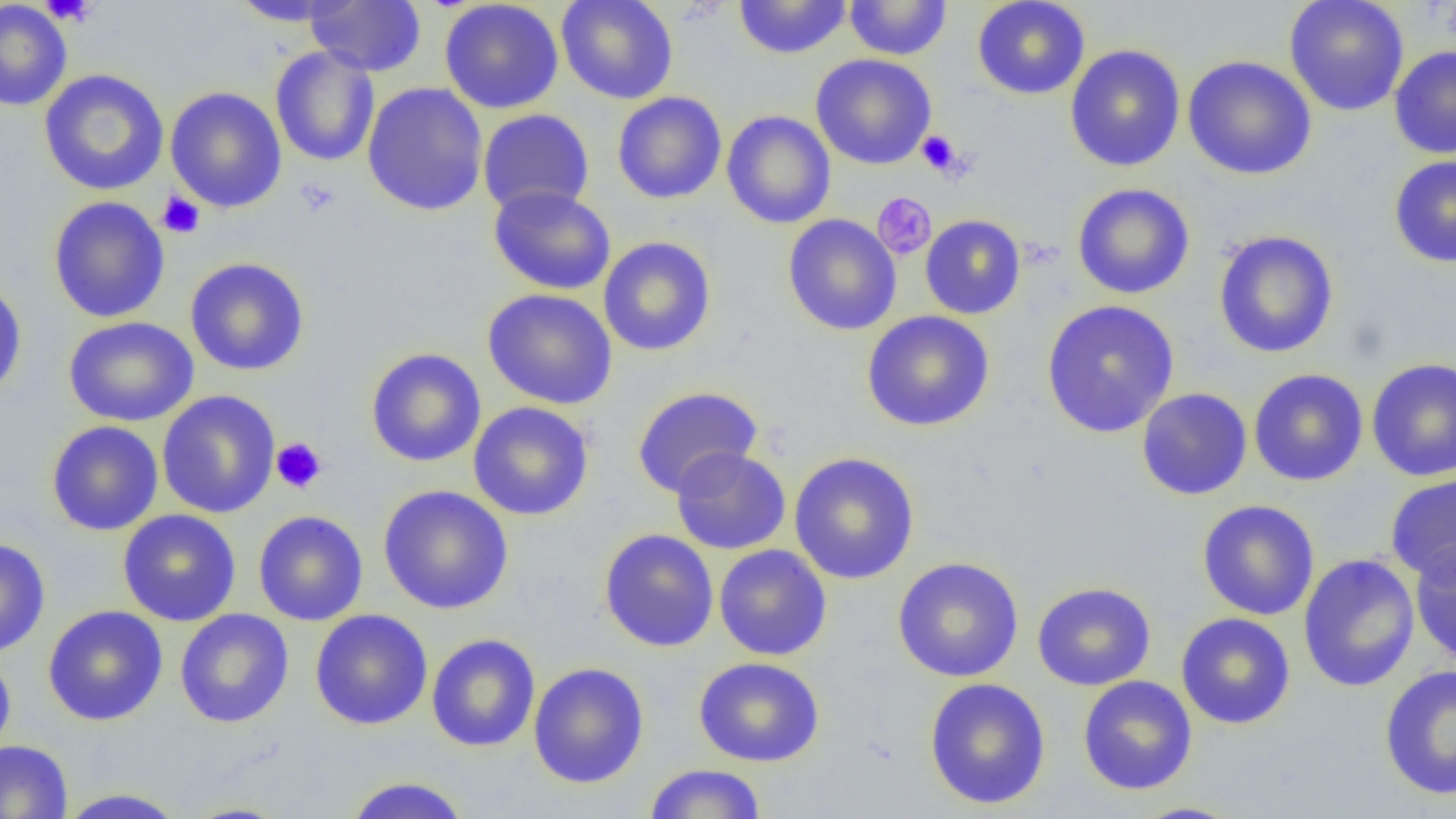

Summary:
  - Coordinate format: approximate bounding boxes as named x1/y1/x2/y2 corners in pixels
  - Uninfected red blood cell locations: (x1=228, y1=0, x2=355, y2=27), (x1=305, y1=0, x2=426, y2=76), (x1=439, y1=0, x2=564, y2=114), (x1=556, y1=0, x2=679, y2=104), (x1=733, y1=0, x2=852, y2=59), (x1=972, y1=0, x2=1091, y2=100), (x1=1284, y1=0, x2=1409, y2=116), (x1=0, y1=1, x2=72, y2=111), (x1=844, y1=1, x2=952, y2=60), (x1=1065, y1=44, x2=1185, y2=172), (x1=270, y1=46, x2=380, y2=166), (x1=1389, y1=46, x2=1456, y2=159), (x1=810, y1=53, x2=937, y2=170), (x1=1182, y1=55, x2=1317, y2=180), (x1=39, y1=69, x2=169, y2=196), (x1=362, y1=82, x2=488, y2=216), (x1=165, y1=86, x2=287, y2=213), (x1=612, y1=91, x2=727, y2=204), (x1=478, y1=109, x2=594, y2=215), (x1=722, y1=110, x2=836, y2=229), (x1=1388, y1=154, x2=1456, y2=268), (x1=1071, y1=182, x2=1196, y2=300), (x1=488, y1=185, x2=616, y2=295), (x1=47, y1=196, x2=170, y2=323), (x1=783, y1=214, x2=902, y2=335), (x1=920, y1=215, x2=1026, y2=319), (x1=1213, y1=230, x2=1339, y2=359), (x1=598, y1=236, x2=716, y2=356), (x1=185, y1=257, x2=310, y2=376), (x1=0, y1=276, x2=27, y2=402), (x1=482, y1=288, x2=618, y2=410), (x1=1040, y1=299, x2=1180, y2=438), (x1=862, y1=310, x2=995, y2=432), (x1=63, y1=316, x2=199, y2=427), (x1=366, y1=348, x2=486, y2=468), (x1=1366, y1=358, x2=1456, y2=481), (x1=1249, y1=368, x2=1368, y2=486), (x1=631, y1=386, x2=763, y2=498), (x1=1137, y1=388, x2=1252, y2=500), (x1=157, y1=390, x2=280, y2=518), (x1=468, y1=401, x2=594, y2=521), (x1=47, y1=420, x2=164, y2=536), (x1=670, y1=447, x2=791, y2=555), (x1=789, y1=452, x2=920, y2=584), (x1=1385, y1=473, x2=1456, y2=585), (x1=378, y1=484, x2=514, y2=614), (x1=1197, y1=499, x2=1320, y2=620), (x1=117, y1=509, x2=241, y2=626), (x1=253, y1=509, x2=368, y2=626), (x1=599, y1=529, x2=718, y2=653), (x1=0, y1=537, x2=51, y2=658), (x1=1409, y1=540, x2=1456, y2=664), (x1=714, y1=544, x2=832, y2=661), (x1=1298, y1=553, x2=1420, y2=693), (x1=892, y1=556, x2=1024, y2=682), (x1=1032, y1=582, x2=1157, y2=691), (x1=42, y1=605, x2=168, y2=726), (x1=174, y1=609, x2=294, y2=728), (x1=310, y1=609, x2=433, y2=730), (x1=1176, y1=612, x2=1296, y2=730), (x1=426, y1=633, x2=540, y2=752), (x1=0, y1=650, x2=16, y2=761), (x1=693, y1=657, x2=825, y2=767), (x1=529, y1=662, x2=649, y2=789), (x1=1379, y1=664, x2=1456, y2=800), (x1=1077, y1=675, x2=1197, y2=795), (x1=923, y1=677, x2=1052, y2=810), (x1=0, y1=739, x2=73, y2=819), (x1=642, y1=763, x2=767, y2=818), (x1=342, y1=776, x2=472, y2=819), (x1=54, y1=787, x2=190, y2=818), (x1=176, y1=801, x2=295, y2=818), (x1=1128, y1=801, x2=1247, y2=819)
  - Platelet locations: (x1=38, y1=0, x2=100, y2=26), (x1=915, y1=130, x2=964, y2=178), (x1=294, y1=178, x2=341, y2=217), (x1=157, y1=191, x2=205, y2=239), (x1=871, y1=192, x2=937, y2=259), (x1=271, y1=437, x2=327, y2=494)
  - Slide-level diagnosis: no evidence of blood parasites
  - Preparation: thin blood smear
  - Magnification: 1000x
  - Modality: optical microscopy
  - Field of view: single
  - Image size: 1456×819 pixels